State which parasite is depicted.
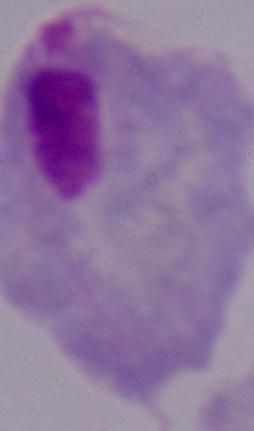

A trichomonad.

Photomicrograph. 1000x magnification.